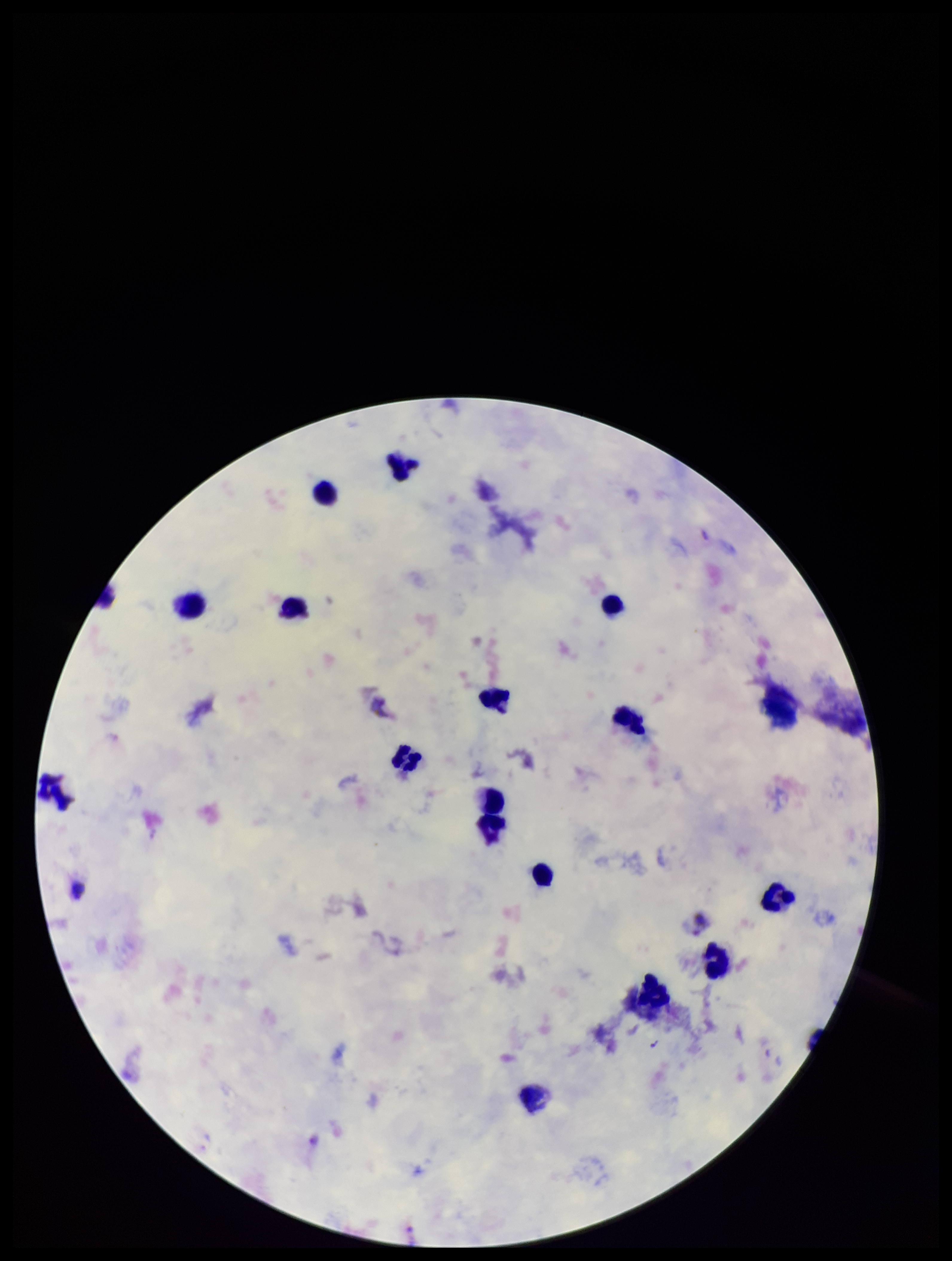
Summary:
  - Field of view: one from this slide
  - Patient malaria status: positive
  - Species reported for this patient: Plasmodium vivax
  - Capture: smartphone photograph through the microscope eyepiece
  - Preparation: thick
  - Plasmodium parasites: none identified
  - Stain: Giemsa
  - Parasite count: 0
  - Leukocyte count: 16
  - Image size: 952×1261 pixels